Assess this cell for malaria.
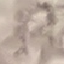
It is uninfected.

Photographed with a smartphone camera at the microscope eyepiece. Cell patch, automatically extracted from a larger field of view and resized to 64 × 64 pixels. Thin blood smear. Giemsa-stained preparation.